Outline each uninfected red blood cell.
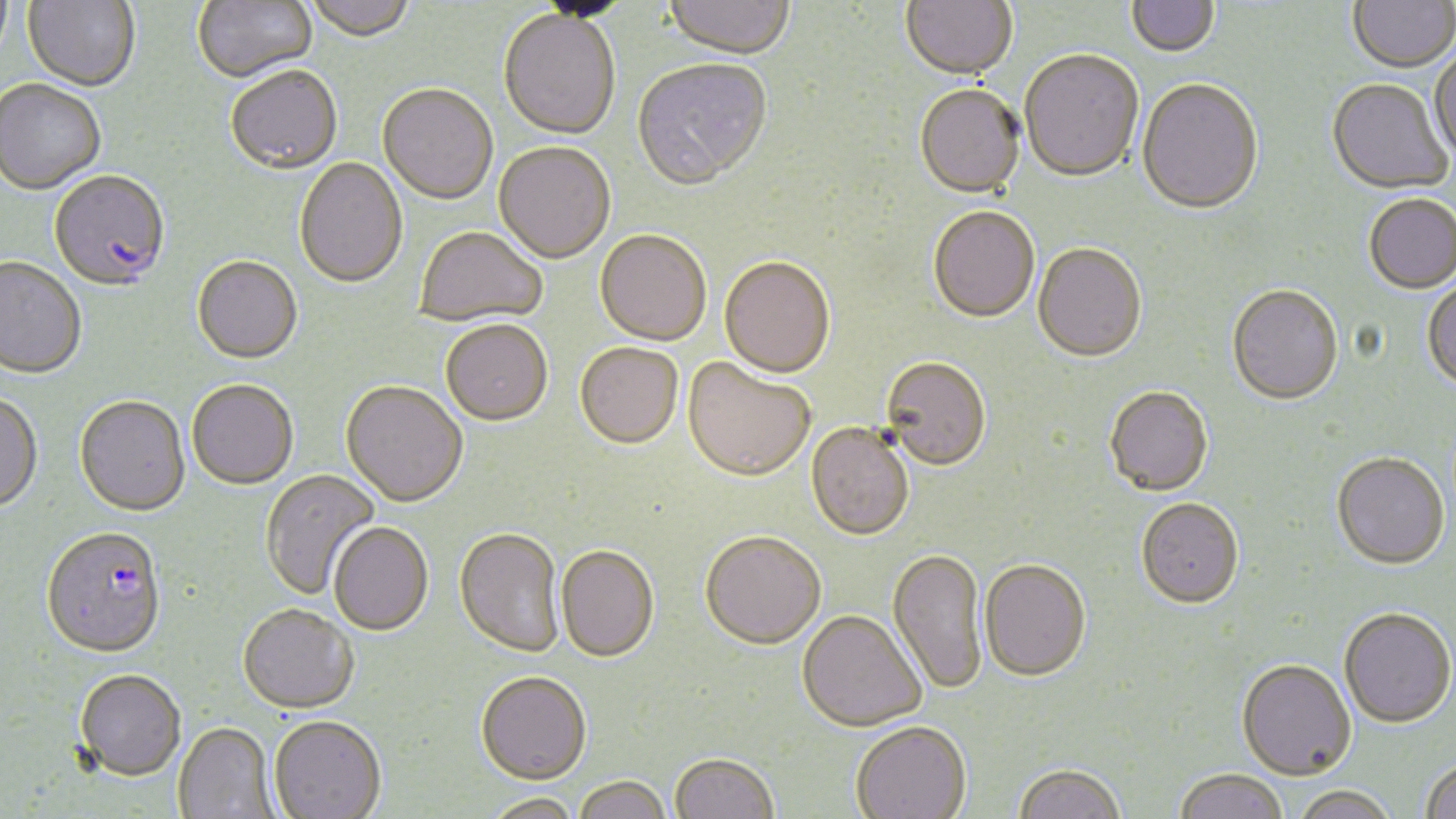
Approximate bounding boxes as (x1, y1, x2, y2) in pixels.
Uninfected red blood cells: (0, 0, 13, 68), (23, 0, 140, 93), (193, 0, 316, 84), (303, 0, 418, 44), (534, 0, 634, 23), (900, 0, 1018, 83), (1126, 0, 1220, 59), (1348, 0, 1456, 75), (662, 1, 795, 63), (498, 12, 621, 142), (1430, 50, 1456, 167), (1019, 52, 1144, 185), (632, 60, 772, 194), (226, 69, 343, 177), (1136, 80, 1264, 218), (1326, 80, 1451, 196), (0, 81, 106, 196), (377, 85, 498, 207), (914, 86, 1025, 201), (493, 143, 615, 266), (294, 159, 408, 291), (1364, 196, 1456, 295), (928, 208, 1040, 325), (415, 227, 548, 328), (594, 232, 712, 348), (1032, 245, 1147, 365), (192, 258, 302, 366), (0, 259, 87, 381), (719, 259, 836, 380), (1423, 279, 1456, 393), (1226, 287, 1343, 408), (441, 323, 553, 429), (575, 345, 683, 452), (682, 359, 815, 485), (881, 359, 991, 474), (187, 382, 298, 491), (340, 383, 468, 509), (1105, 389, 1213, 498), (0, 394, 43, 514), (75, 397, 190, 518), (805, 424, 914, 543), (1332, 455, 1450, 572), (260, 469, 381, 601), (1136, 500, 1244, 612), (328, 524, 433, 637), (453, 529, 565, 659), (700, 534, 826, 653), (555, 547, 659, 664), (886, 550, 989, 697), (979, 562, 1091, 685), (237, 605, 359, 716), (1339, 610, 1455, 730), (797, 612, 926, 734), (1236, 661, 1356, 783), (75, 671, 186, 783), (476, 674, 592, 787), (268, 717, 386, 819), (850, 723, 971, 819), (173, 724, 279, 818), (669, 755, 778, 819), (1420, 760, 1456, 819), (1012, 765, 1127, 819), (1173, 771, 1288, 819), (573, 778, 672, 819), (1290, 788, 1399, 818), (480, 794, 585, 819).

slide-level diagnosis = Plasmodium falciparum
magnification = 1000x
field of view = one of a larger specimen
Plasmodium falciparum-infected red blood cell locations = approximate bounding boxes as (x1, y1, x2, y2) in pixels: (48, 172, 171, 294), (41, 528, 167, 661)
image size = 1456×819 pixels
preparation = thin blood smear
stain = May-Grünwald-Giemsa
modality = optical microscopy